Name the parasite shown.
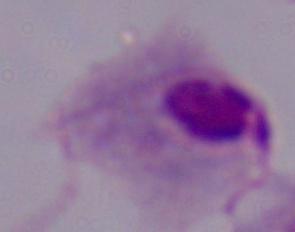

This is a trichomonad.

Micrograph. Captured at 1000x magnification.